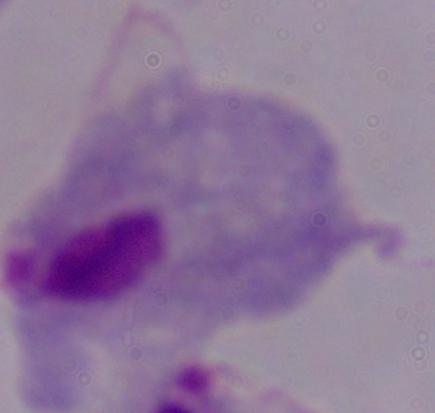
Photomicrograph. A trichomonad is shown. 1000x magnification.